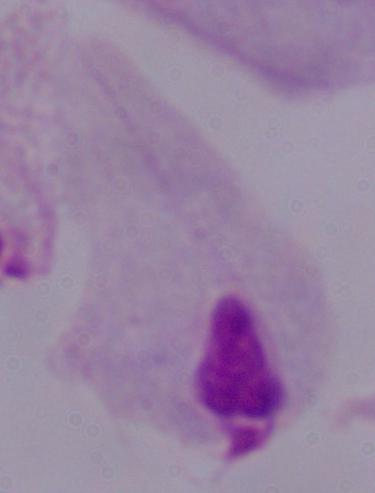 Captured at 1000x magnification. A trichomonad is seen. Photomicrograph.